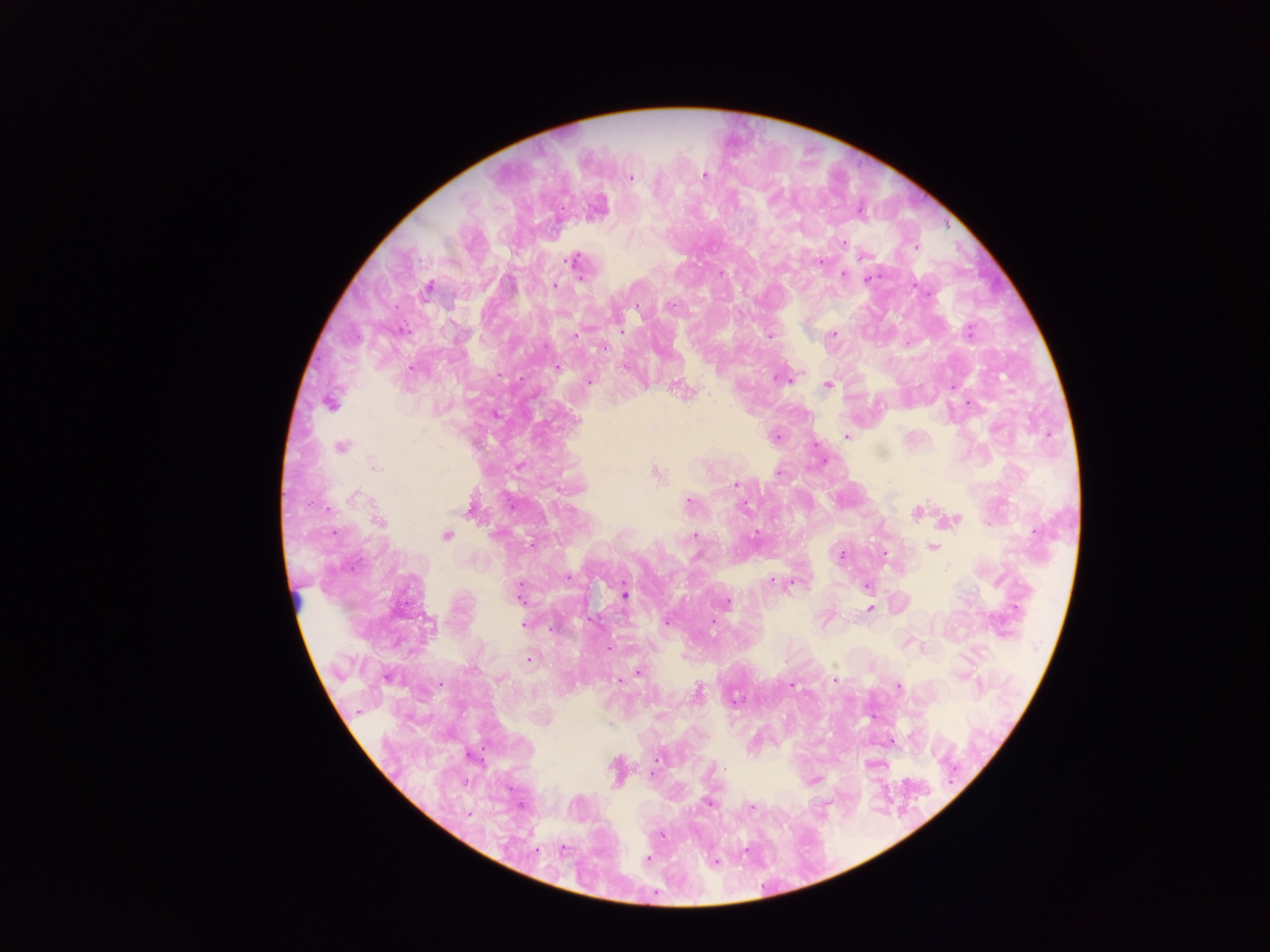
leukocyte locations = approximate centers as {x, y} in pixels: {296, 598}
image size = 1270×952 pixels
capture = mobile-phone photograph through a microscope
country = Ghana
preparation = thick blood film
Plasmodium parasite locations = approximate centers as {x, y} in pixels: {704, 175}, {630, 177}, {843, 244}, {915, 246}, {864, 255}, {573, 260}, {819, 262}, {721, 273}, {843, 275}, {582, 279}, {868, 279}, {554, 285}, {428, 288}, {670, 305}, {637, 307}, {621, 331}, {969, 331}, {833, 334}, {575, 335}, {769, 336}, {604, 346}, {624, 367}, {557, 368}, {787, 379}, {589, 381}, {827, 385}, {677, 386}, {330, 403}, {846, 437}, {341, 446}, {375, 466}, {657, 473}, {737, 485}, {355, 497}, {689, 502}, {470, 511}, {917, 512}, {954, 519}, {379, 522}, {755, 534}, {694, 535}, {447, 536}, {932, 547}, {884, 554}, {841, 556}, {568, 578}, {772, 581}, {794, 581}, {867, 586}, {518, 591}, {624, 594}, {727, 603}, {870, 609}, {712, 621}, {667, 622}, {524, 625}, {906, 643}, {609, 649}, {529, 659}, {638, 672}, {618, 680}, {836, 680}, {439, 684}, {792, 685}, {899, 686}, {698, 692}, {657, 760}, {708, 803}, {751, 807}, {469, 814}, {562, 850}, {648, 859}, {715, 863}
field of view = single